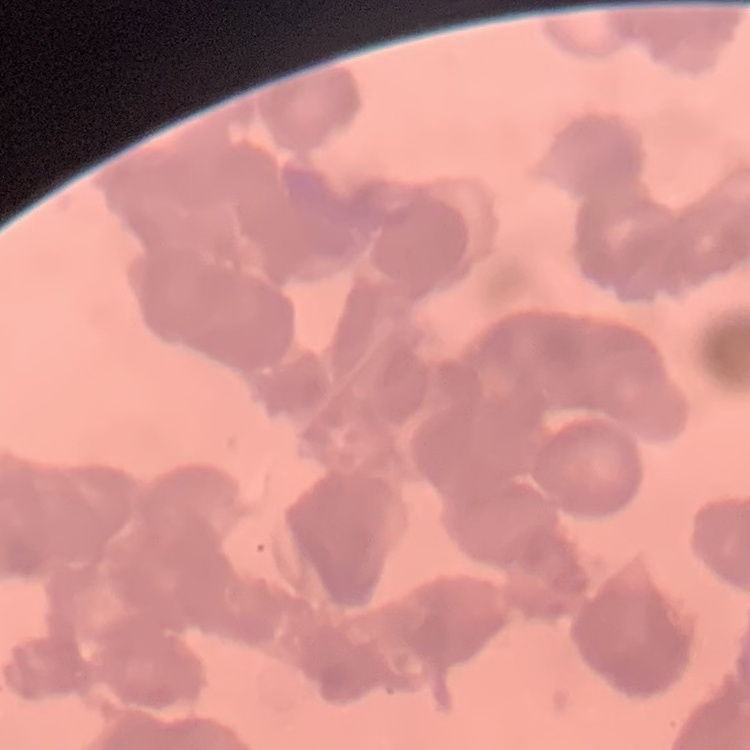 The erythrocytes exhibit rouleaux formation. Field's or Giemsa stain. Square crop of a larger photomicrograph. Thin peripheral smear.